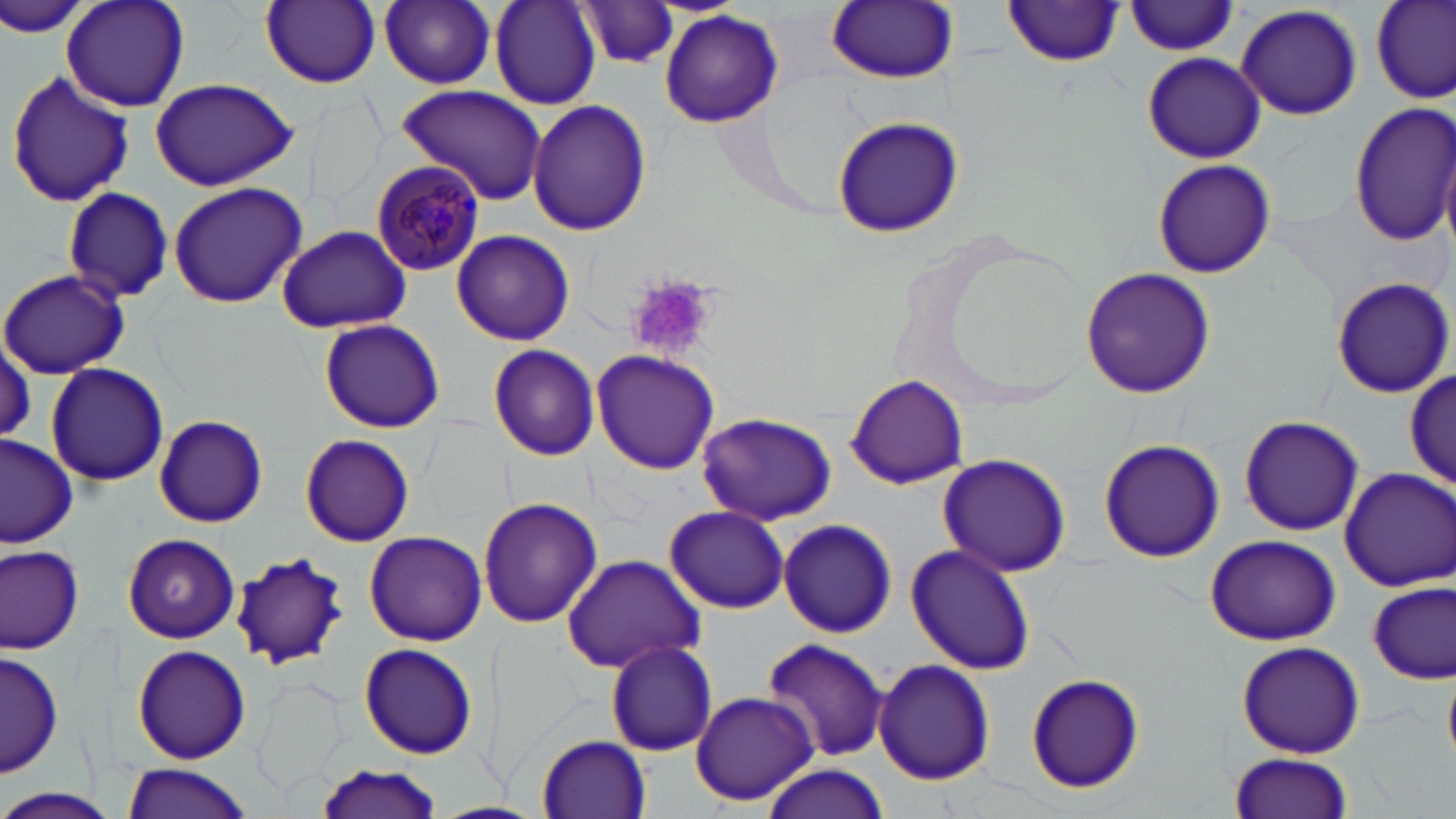

slide-level diagnosis = Plasmodium malariae
image size = 1456×819 pixels
uninfected red blood cell locations = approximate bounding boxes as (x1, y1, x2, y2) in pixels: (0, 0, 96, 44), (61, 0, 190, 110), (261, 0, 381, 88), (378, 0, 504, 91), (490, 0, 600, 109), (1372, 0, 1456, 104), (573, 2, 686, 71), (826, 2, 958, 84), (1001, 2, 1126, 67), (1124, 3, 1240, 56), (1236, 3, 1362, 122), (660, 10, 782, 127), (1142, 51, 1265, 164), (6, 68, 137, 210), (149, 77, 300, 192), (397, 85, 549, 206), (527, 100, 652, 235), (1349, 100, 1456, 248), (831, 115, 963, 239), (1151, 158, 1276, 279), (168, 181, 308, 308), (60, 186, 175, 304), (276, 224, 412, 334), (452, 230, 575, 346), (1081, 266, 1215, 399), (1, 268, 129, 378), (1330, 276, 1453, 397), (319, 318, 445, 433), (486, 344, 601, 462), (592, 349, 721, 475), (44, 360, 169, 485), (1404, 366, 1453, 493), (846, 378, 967, 490), (697, 412, 837, 526), (154, 414, 269, 528), (1238, 414, 1364, 536), (0, 434, 78, 548), (298, 434, 414, 545), (1098, 438, 1227, 562), (937, 452, 1072, 575), (1337, 467, 1455, 591), (479, 496, 601, 628), (665, 506, 791, 614), (779, 518, 898, 639), (364, 530, 487, 645), (122, 533, 242, 643), (1203, 535, 1343, 645), (906, 542, 1035, 676), (0, 544, 86, 653), (231, 550, 348, 670), (561, 554, 706, 674), (1368, 581, 1454, 683), (763, 636, 890, 763), (1236, 641, 1365, 759), (604, 642, 719, 756), (130, 644, 252, 764), (359, 644, 478, 759), (2, 648, 62, 779), (872, 658, 995, 787), (1026, 671, 1144, 793), (252, 676, 346, 796), (689, 690, 819, 808), (536, 734, 651, 816), (1227, 752, 1353, 819), (308, 758, 446, 819), (120, 762, 255, 818), (756, 764, 889, 818), (0, 790, 120, 819)
field of view = single
Plasmodium malariae-infected red blood cell locations = approximate bounding boxes as (x1, y1, x2, y2) in pixels: (370, 160, 486, 277)
modality = optical microscopy
stain = May-Grünwald-Giemsa
preparation = thin blood smear
platelet locations = approximate bounding boxes as (x1, y1, x2, y2) in pixels: (631, 276, 723, 360)
magnification = 1000x